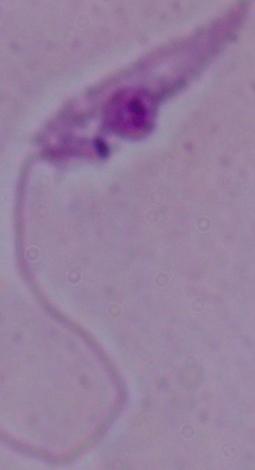

modality = photomicrograph
magnification = 1000x
identification = Leishmania